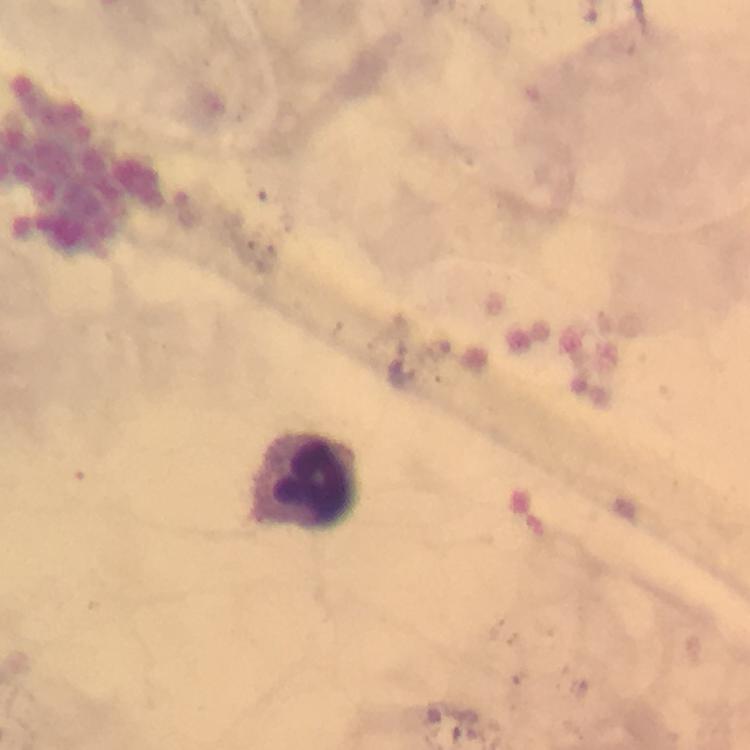
Approximate centers as {x, y} in pixels. Leukocyte locations: {306, 481}. Photographed through the microscope with a smartphone camera. Thick blood film. Giemsa stain. Malaria parasites: none detected. From a malaria diagnostic workup. Image is 750×750 pixels. Immersion oil applied. Cropped region of a single field of view. At 100x magnification.